Give the extent of all Plasmodium falciparum-infected red blood cells.
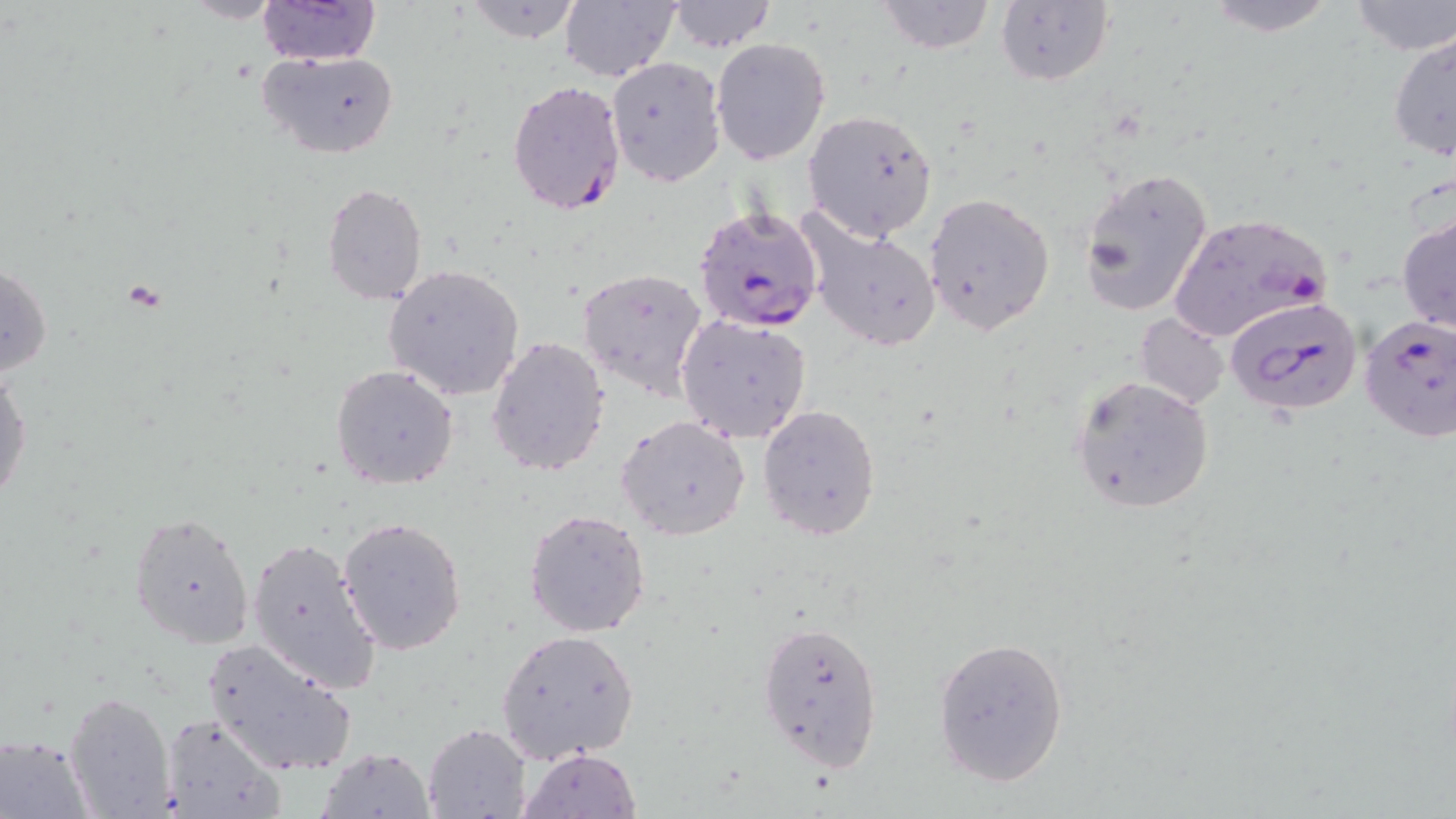

Approximate bounding boxes as [x1, y1, x2, y2] in pixels.
Plasmodium falciparum-infected red blood cells: [506, 79, 627, 217], [693, 206, 825, 334], [1166, 212, 1332, 344], [1226, 296, 1364, 417], [1358, 316, 1456, 441].

Uninfected red blood cell locations: [179, 0, 285, 23], [459, 0, 587, 44], [560, 0, 680, 82], [876, 0, 995, 54], [994, 0, 1115, 90], [1200, 0, 1342, 37], [1345, 0, 1456, 55], [258, 1, 381, 67], [667, 1, 776, 53], [1387, 29, 1456, 163], [711, 37, 831, 166], [258, 50, 400, 159], [606, 57, 724, 185], [802, 108, 939, 243], [1080, 165, 1215, 315], [321, 183, 428, 304], [923, 192, 1055, 336], [1396, 209, 1456, 336], [801, 213, 943, 353], [2, 260, 52, 378], [383, 265, 524, 400], [577, 265, 710, 403], [675, 314, 813, 444], [1135, 314, 1229, 406], [487, 335, 611, 476], [0, 365, 32, 511], [331, 365, 459, 489], [1070, 376, 1215, 516], [758, 405, 883, 542], [616, 416, 751, 540], [523, 508, 651, 638], [130, 510, 255, 648], [338, 517, 468, 655], [247, 536, 381, 695], [756, 619, 884, 772], [496, 629, 640, 763], [932, 635, 1070, 787], [203, 636, 357, 777], [64, 691, 174, 818], [159, 712, 284, 819], [423, 722, 532, 819], [1, 734, 95, 816], [319, 746, 434, 818], [518, 748, 640, 819]. Slide-level diagnosis: Plasmodium falciparum. Image is 1456×819 pixels. Thin blood smear. One field of a larger specimen. Captured at 1000x magnification. May-Grünwald-Giemsa stain. Optical microscopy.